Assess for malaria.
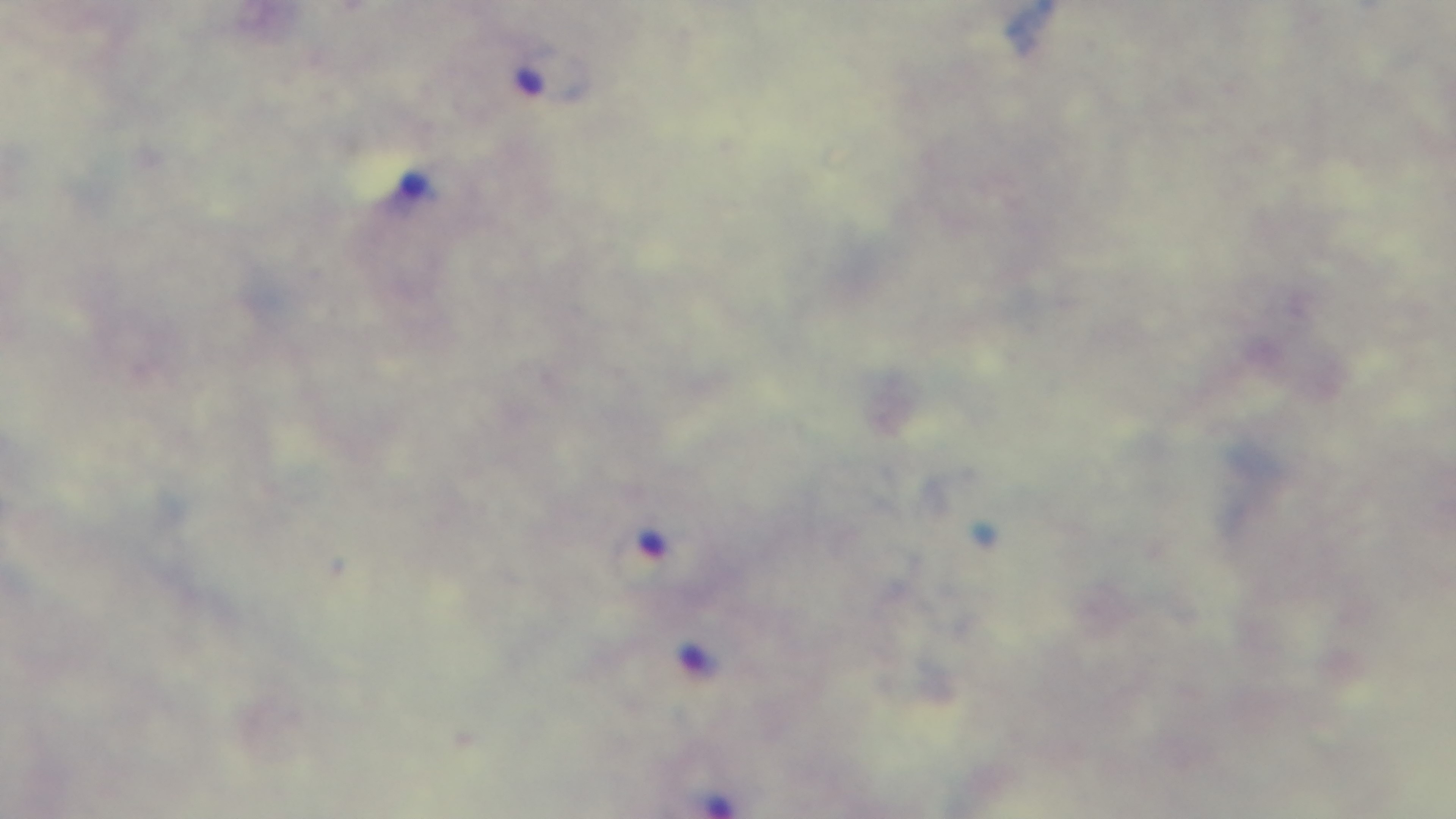

Infected.

Mounted 4K digital camera. Preparation: thick. Oil-immersion objective, 100x. Giemsa-stained. Single field of view. Light microscopy.